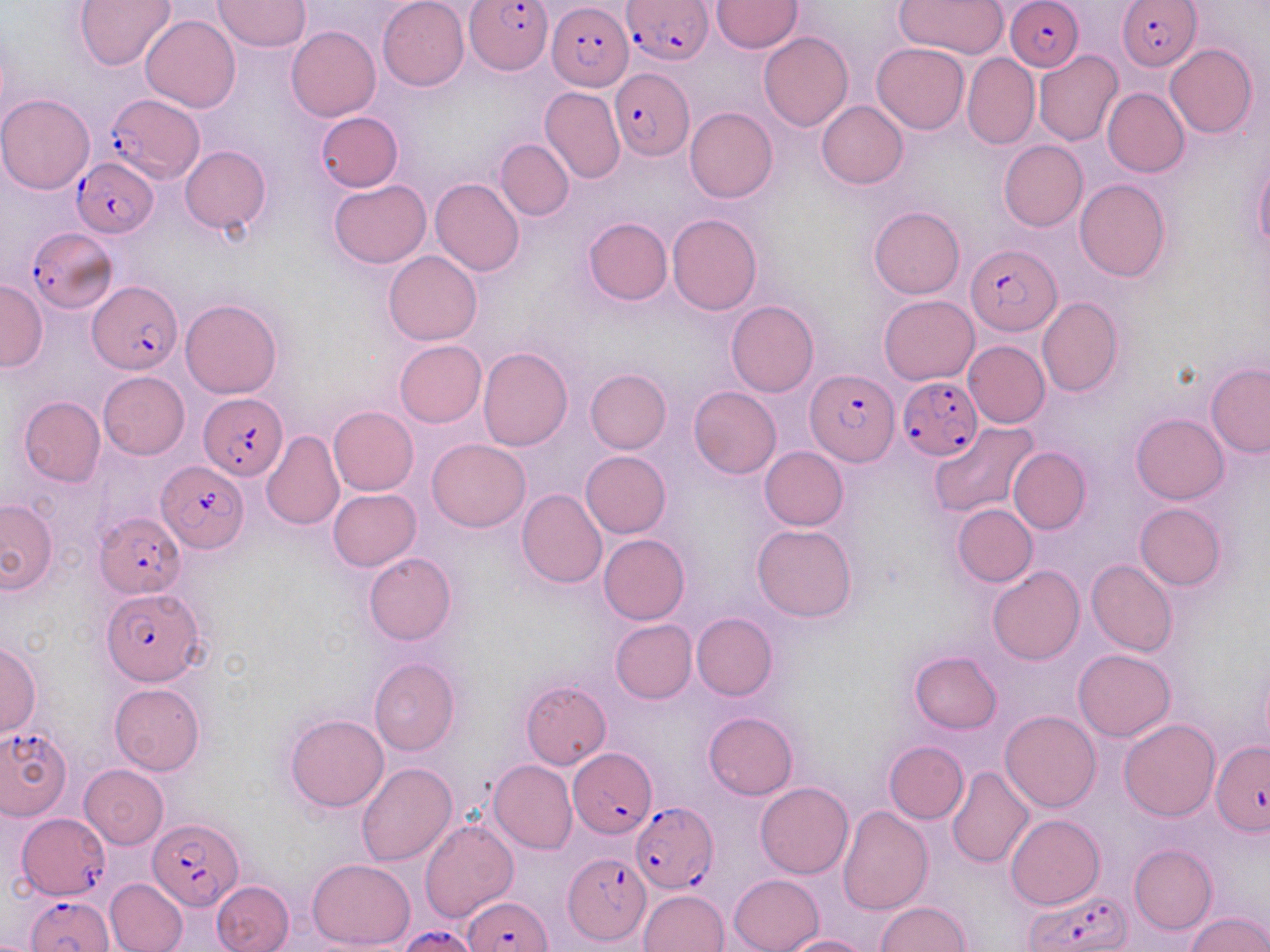

Summary:
  - Coordinate format: approximate bounding boxes as named x1/y1/x2/y2 corners in pixels
  - Uninfected red blood cell locations: (x1=378, y1=0, x2=468, y2=91), (x1=712, y1=0, x2=801, y2=53), (x1=73, y1=1, x2=176, y2=72), (x1=214, y1=1, x2=310, y2=52), (x1=894, y1=1, x2=1007, y2=58), (x1=141, y1=13, x2=240, y2=113), (x1=287, y1=26, x2=380, y2=122), (x1=759, y1=32, x2=853, y2=131), (x1=872, y1=43, x2=969, y2=134), (x1=1166, y1=44, x2=1257, y2=138), (x1=1034, y1=50, x2=1123, y2=147), (x1=962, y1=53, x2=1039, y2=149), (x1=540, y1=86, x2=625, y2=184), (x1=1103, y1=87, x2=1189, y2=177), (x1=0, y1=94, x2=95, y2=193), (x1=817, y1=101, x2=907, y2=188), (x1=685, y1=107, x2=778, y2=202), (x1=315, y1=112, x2=403, y2=193), (x1=495, y1=140, x2=574, y2=220), (x1=998, y1=140, x2=1088, y2=232), (x1=180, y1=145, x2=271, y2=235), (x1=1255, y1=158, x2=1270, y2=252), (x1=430, y1=177, x2=524, y2=276), (x1=1075, y1=178, x2=1171, y2=281), (x1=328, y1=181, x2=431, y2=268), (x1=869, y1=206, x2=965, y2=298), (x1=667, y1=214, x2=761, y2=315), (x1=583, y1=218, x2=672, y2=305), (x1=383, y1=251, x2=482, y2=345), (x1=0, y1=281, x2=47, y2=370), (x1=878, y1=295, x2=978, y2=384), (x1=1036, y1=296, x2=1124, y2=398), (x1=180, y1=298, x2=283, y2=399), (x1=726, y1=300, x2=819, y2=397), (x1=394, y1=340, x2=486, y2=427), (x1=963, y1=340, x2=1050, y2=429), (x1=477, y1=347, x2=572, y2=451), (x1=1206, y1=363, x2=1270, y2=456), (x1=585, y1=368, x2=671, y2=453), (x1=98, y1=372, x2=189, y2=459), (x1=689, y1=387, x2=781, y2=479), (x1=18, y1=396, x2=105, y2=486), (x1=328, y1=406, x2=418, y2=495), (x1=1131, y1=413, x2=1228, y2=504), (x1=928, y1=421, x2=1039, y2=520), (x1=261, y1=429, x2=344, y2=530), (x1=426, y1=439, x2=531, y2=532), (x1=759, y1=447, x2=849, y2=530), (x1=1009, y1=447, x2=1090, y2=532), (x1=580, y1=450, x2=670, y2=538), (x1=516, y1=488, x2=607, y2=588), (x1=327, y1=489, x2=422, y2=571), (x1=0, y1=498, x2=58, y2=593), (x1=1134, y1=502, x2=1226, y2=591), (x1=953, y1=504, x2=1037, y2=586), (x1=752, y1=524, x2=857, y2=623), (x1=599, y1=534, x2=690, y2=624), (x1=364, y1=553, x2=456, y2=645), (x1=1087, y1=560, x2=1177, y2=657), (x1=987, y1=565, x2=1085, y2=664), (x1=691, y1=613, x2=777, y2=701), (x1=610, y1=619, x2=697, y2=703), (x1=1, y1=643, x2=41, y2=737), (x1=1072, y1=649, x2=1175, y2=740), (x1=909, y1=651, x2=1002, y2=734), (x1=369, y1=658, x2=460, y2=756), (x1=520, y1=680, x2=612, y2=769), (x1=109, y1=683, x2=204, y2=774), (x1=1001, y1=710, x2=1101, y2=813), (x1=703, y1=712, x2=798, y2=800), (x1=284, y1=713, x2=389, y2=812), (x1=1119, y1=718, x2=1220, y2=821), (x1=884, y1=741, x2=968, y2=823), (x1=489, y1=760, x2=577, y2=854), (x1=357, y1=762, x2=457, y2=866), (x1=79, y1=764, x2=169, y2=849), (x1=947, y1=765, x2=1034, y2=869), (x1=755, y1=782, x2=853, y2=879), (x1=836, y1=806, x2=933, y2=916), (x1=1007, y1=814, x2=1104, y2=909), (x1=420, y1=818, x2=518, y2=921), (x1=1129, y1=843, x2=1217, y2=934), (x1=307, y1=858, x2=416, y2=949), (x1=729, y1=874, x2=823, y2=952), (x1=106, y1=878, x2=189, y2=952), (x1=211, y1=880, x2=293, y2=952), (x1=639, y1=889, x2=728, y2=952), (x1=876, y1=901, x2=970, y2=951), (x1=1187, y1=910, x2=1270, y2=951), (x1=782, y1=935, x2=873, y2=952)
  - Plasmodium falciparum-infected red blood cell locations: (x1=464, y1=0, x2=553, y2=76), (x1=621, y1=0, x2=714, y2=67), (x1=1007, y1=0, x2=1085, y2=72), (x1=1119, y1=0, x2=1200, y2=70), (x1=546, y1=3, x2=633, y2=90), (x1=611, y1=69, x2=694, y2=159), (x1=104, y1=96, x2=204, y2=181), (x1=72, y1=159, x2=158, y2=238), (x1=24, y1=228, x2=117, y2=312), (x1=966, y1=245, x2=1062, y2=336), (x1=88, y1=280, x2=182, y2=375), (x1=807, y1=370, x2=899, y2=466), (x1=898, y1=376, x2=981, y2=462), (x1=202, y1=396, x2=287, y2=479), (x1=156, y1=459, x2=247, y2=552), (x1=97, y1=513, x2=186, y2=597), (x1=101, y1=587, x2=204, y2=685), (x1=0, y1=727, x2=72, y2=820), (x1=1212, y1=739, x2=1270, y2=833), (x1=568, y1=748, x2=655, y2=838), (x1=632, y1=801, x2=717, y2=893), (x1=16, y1=814, x2=109, y2=899), (x1=148, y1=818, x2=245, y2=909), (x1=563, y1=851, x2=652, y2=944), (x1=1023, y1=890, x2=1131, y2=952), (x1=27, y1=893, x2=114, y2=952), (x1=464, y1=895, x2=551, y2=951), (x1=398, y1=925, x2=481, y2=952)
  - Slide-level diagnosis: Plasmodium falciparum
  - Field of view: single
  - Magnification: 1000x
  - Image size: 1270×952 pixels
  - Modality: optical microscopy
  - Preparation: thin blood smear
  - Stain: May-Grünwald-Giemsa